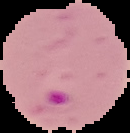 Malaria status: parasitized. From a thin blood smear. Cell region segmented out of the field of view; the surrounding area is masked to black. Image is 130×133 pixels.